Outline each uninfected red blood cell.
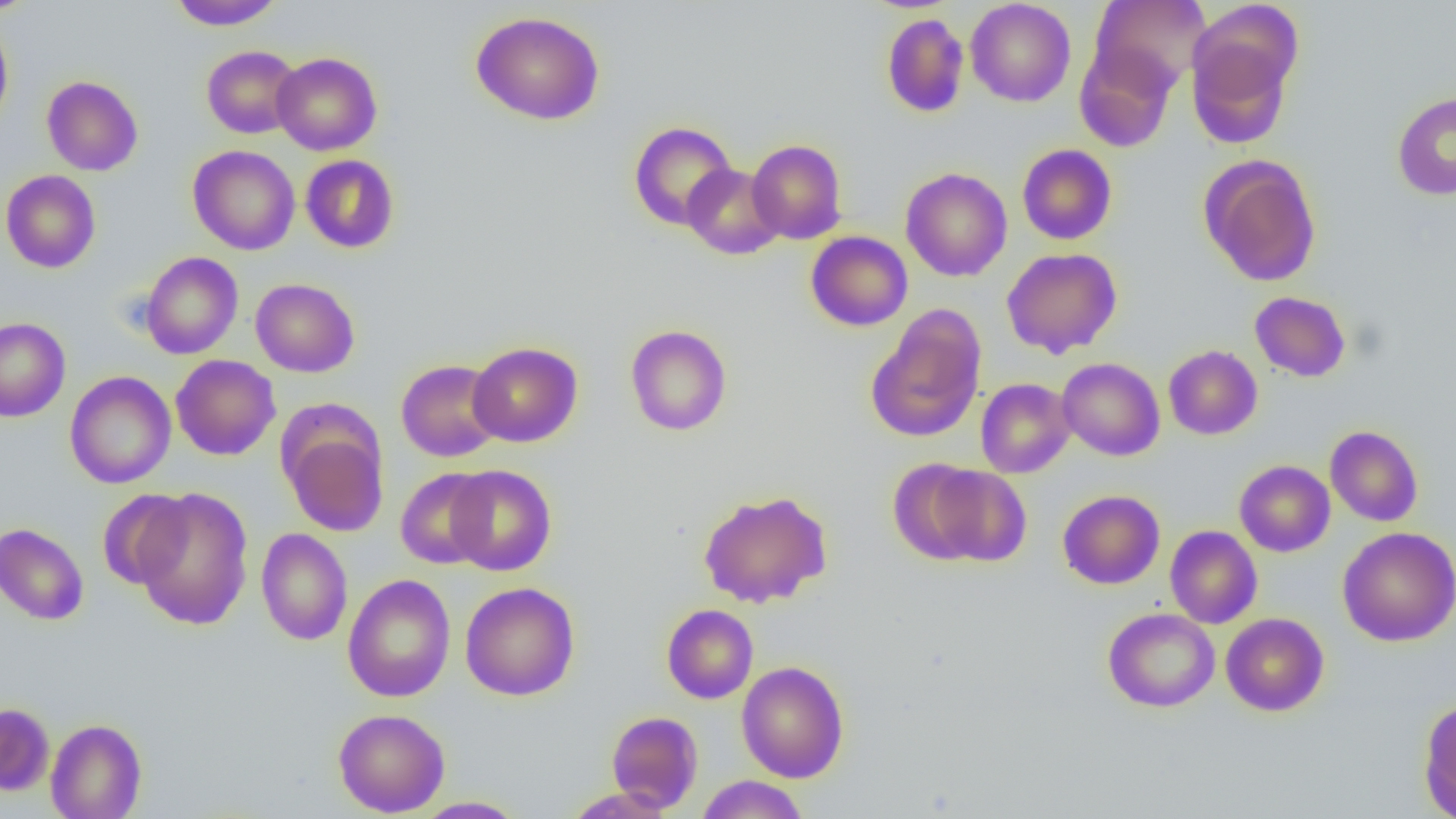
Approximate bounding boxes as named x1/y1/x2/y2 corners in pixels.
Uninfected red blood cells: (x1=0, y1=0, x2=41, y2=17), (x1=168, y1=0, x2=286, y2=30), (x1=965, y1=0, x2=1076, y2=107), (x1=1090, y1=0, x2=1212, y2=91), (x1=471, y1=11, x2=605, y2=125), (x1=881, y1=13, x2=970, y2=118), (x1=0, y1=19, x2=13, y2=133), (x1=1186, y1=30, x2=1296, y2=149), (x1=1074, y1=43, x2=1179, y2=153), (x1=202, y1=45, x2=302, y2=139), (x1=271, y1=52, x2=382, y2=155), (x1=41, y1=75, x2=143, y2=175), (x1=1392, y1=92, x2=1456, y2=200), (x1=628, y1=121, x2=738, y2=230), (x1=747, y1=139, x2=847, y2=244), (x1=1017, y1=144, x2=1117, y2=245), (x1=188, y1=145, x2=301, y2=255), (x1=300, y1=154, x2=399, y2=253), (x1=1200, y1=154, x2=1321, y2=287), (x1=682, y1=163, x2=785, y2=260), (x1=900, y1=167, x2=1013, y2=282), (x1=1, y1=170, x2=101, y2=273), (x1=805, y1=231, x2=912, y2=331), (x1=1002, y1=248, x2=1122, y2=358), (x1=140, y1=251, x2=243, y2=359), (x1=250, y1=278, x2=360, y2=377), (x1=1249, y1=291, x2=1351, y2=382), (x1=866, y1=308, x2=987, y2=444), (x1=0, y1=317, x2=70, y2=422), (x1=625, y1=323, x2=732, y2=436), (x1=468, y1=342, x2=582, y2=447), (x1=1163, y1=345, x2=1262, y2=440), (x1=170, y1=355, x2=281, y2=460), (x1=1057, y1=357, x2=1165, y2=461), (x1=396, y1=359, x2=505, y2=462), (x1=64, y1=371, x2=176, y2=489), (x1=976, y1=378, x2=1075, y2=478), (x1=280, y1=418, x2=389, y2=537), (x1=1325, y1=425, x2=1423, y2=526), (x1=887, y1=458, x2=989, y2=564), (x1=1234, y1=460, x2=1335, y2=557), (x1=921, y1=464, x2=1032, y2=566), (x1=445, y1=465, x2=557, y2=576), (x1=395, y1=467, x2=495, y2=569), (x1=132, y1=487, x2=254, y2=631), (x1=96, y1=488, x2=192, y2=590), (x1=698, y1=489, x2=832, y2=608), (x1=1057, y1=489, x2=1165, y2=589), (x1=0, y1=523, x2=89, y2=625), (x1=1165, y1=525, x2=1263, y2=628), (x1=1339, y1=526, x2=1456, y2=647), (x1=256, y1=528, x2=353, y2=646), (x1=342, y1=573, x2=456, y2=702), (x1=460, y1=581, x2=580, y2=701), (x1=662, y1=603, x2=758, y2=704), (x1=1103, y1=607, x2=1220, y2=712), (x1=1220, y1=613, x2=1329, y2=716), (x1=735, y1=660, x2=850, y2=783), (x1=1418, y1=698, x2=1456, y2=819), (x1=0, y1=703, x2=54, y2=795), (x1=333, y1=709, x2=449, y2=816), (x1=606, y1=710, x2=703, y2=812), (x1=45, y1=718, x2=147, y2=819), (x1=696, y1=775, x2=809, y2=818), (x1=562, y1=786, x2=678, y2=818), (x1=412, y1=796, x2=527, y2=818).

Slide-level diagnosis: negative for blood parasites. 1000x magnification. Optical microscopy. Image is 1456×819 pixels. Thin blood film. Single field of view.